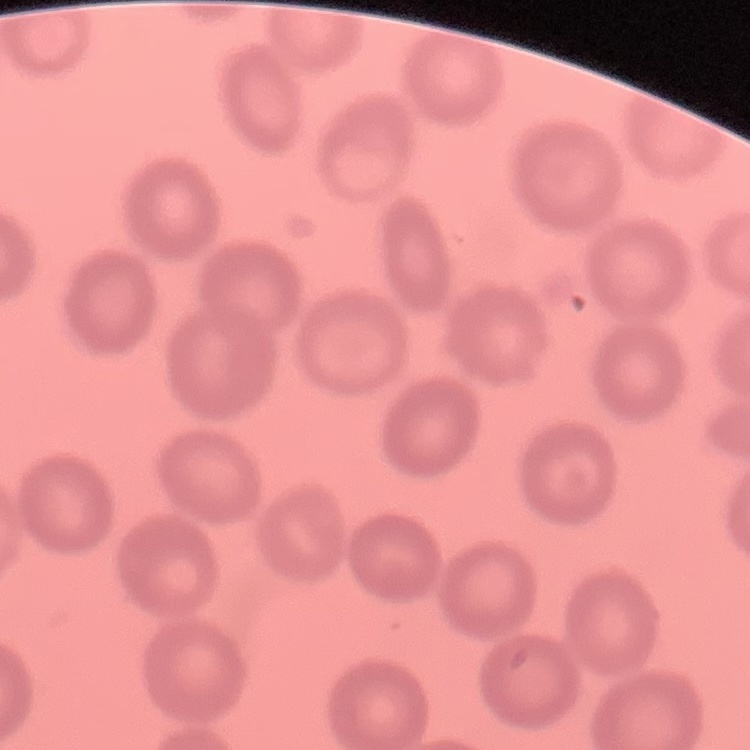

red_blood_cell_morphology: no rouleaux formation
stain: Field's or Giemsa
image_type: square crop of a larger photomicrograph
preparation: thin blood smear